Locate every Plasmodium parasite.
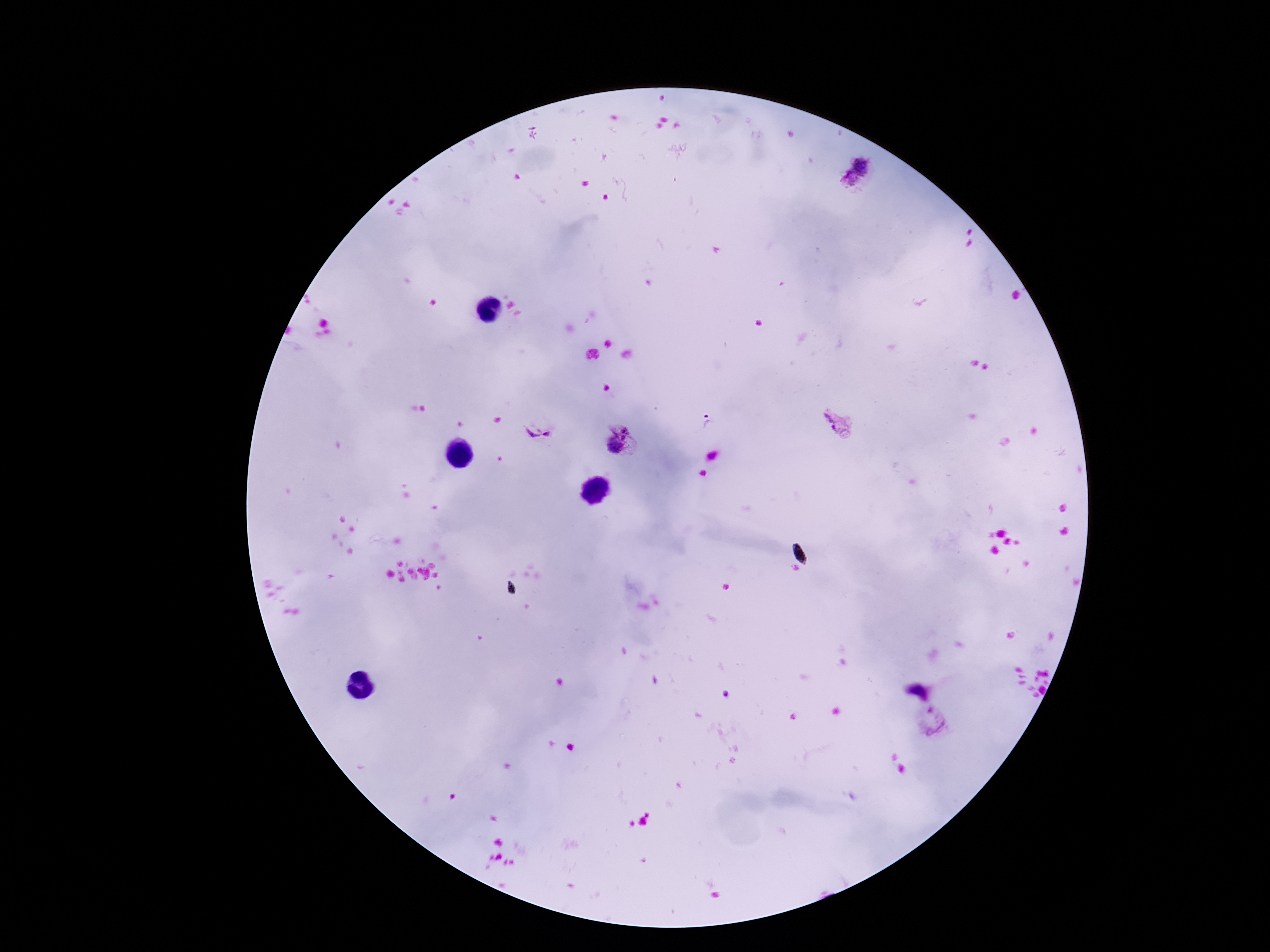

Approximate centers as (x, y) in pixels.
Plasmodium parasites: (857, 170), (707, 421), (837, 424), (540, 431), (621, 442), (933, 722).

Thick blood smear. One field from this slide. 100x magnification. Photographed through the microscope eyepiece with a smartphone camera. Patient malaria status: positive. Giemsa stain. Image is 1270×952 pixels.